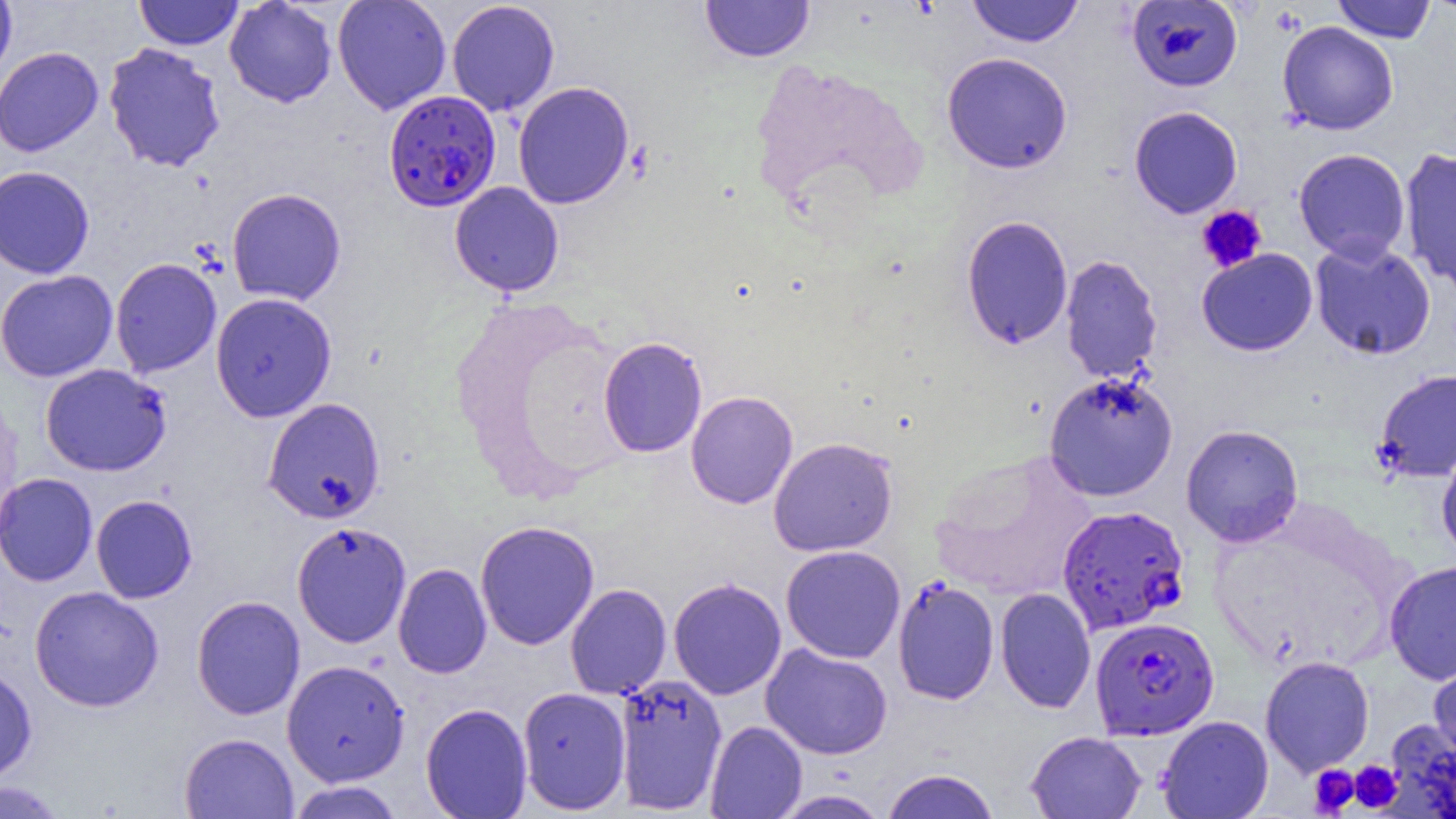
slide-level diagnosis = Plasmodium falciparum
uninfected red blood cell locations = approximate bounding boxes as [x1, y1, x2, y2] in pixels: [0, 0, 17, 87], [134, 0, 243, 50], [224, 0, 338, 108], [332, 0, 452, 115], [700, 0, 815, 62], [967, 0, 1085, 47], [1126, 0, 1243, 92], [1332, 0, 1436, 43], [1423, 0, 1456, 16], [446, 1, 560, 117], [1277, 21, 1398, 135], [103, 42, 227, 172], [0, 46, 104, 157], [942, 52, 1073, 174], [512, 81, 634, 209], [1129, 106, 1243, 218], [1399, 146, 1456, 290], [1294, 148, 1410, 263], [0, 165, 95, 279], [449, 182, 564, 297], [227, 187, 346, 305], [960, 215, 1073, 349], [1309, 239, 1436, 360], [1197, 248, 1318, 356], [1060, 254, 1163, 384], [110, 258, 222, 377], [0, 269, 118, 382], [210, 292, 337, 422], [597, 336, 707, 458], [39, 364, 172, 476], [1373, 368, 1456, 482], [1043, 371, 1179, 502], [685, 391, 798, 509], [262, 397, 386, 524], [1181, 424, 1304, 547], [768, 437, 898, 556], [1436, 442, 1456, 562], [929, 450, 1099, 602], [0, 472, 98, 586], [91, 494, 198, 604], [475, 520, 600, 650], [291, 521, 412, 649], [780, 545, 906, 663], [1384, 560, 1456, 685], [393, 563, 492, 679], [892, 576, 1000, 705], [668, 577, 787, 700], [565, 583, 672, 700], [29, 585, 164, 712], [995, 587, 1096, 714], [191, 595, 306, 720], [761, 643, 893, 759], [1428, 654, 1456, 769], [1260, 656, 1374, 776], [282, 659, 410, 786], [0, 664, 37, 784], [613, 673, 728, 815], [517, 686, 631, 815], [420, 703, 532, 818], [1157, 715, 1273, 819], [1387, 719, 1456, 818], [704, 721, 807, 818], [1025, 731, 1147, 819], [179, 732, 299, 818], [880, 769, 1000, 819], [0, 779, 69, 818], [286, 780, 405, 819], [770, 789, 893, 818]
image size = 1456×819 pixels
preparation = thin blood smear
platelet locations = approximate bounding boxes as [x1, y1, x2, y2] in pixels: [1196, 205, 1267, 273], [1350, 760, 1402, 812], [1308, 765, 1359, 816]
field of view = single
modality = light microscopy
magnification = 1000x
Plasmodium falciparum-infected red blood cell locations = approximate bounding boxes as [x1, y1, x2, y2] in pixels: [383, 89, 501, 211], [1057, 505, 1189, 635], [1089, 616, 1219, 740]